Give the position of every Plasmodium parasite, noting whether each is a trophozoite, schizont, or gametocyte.
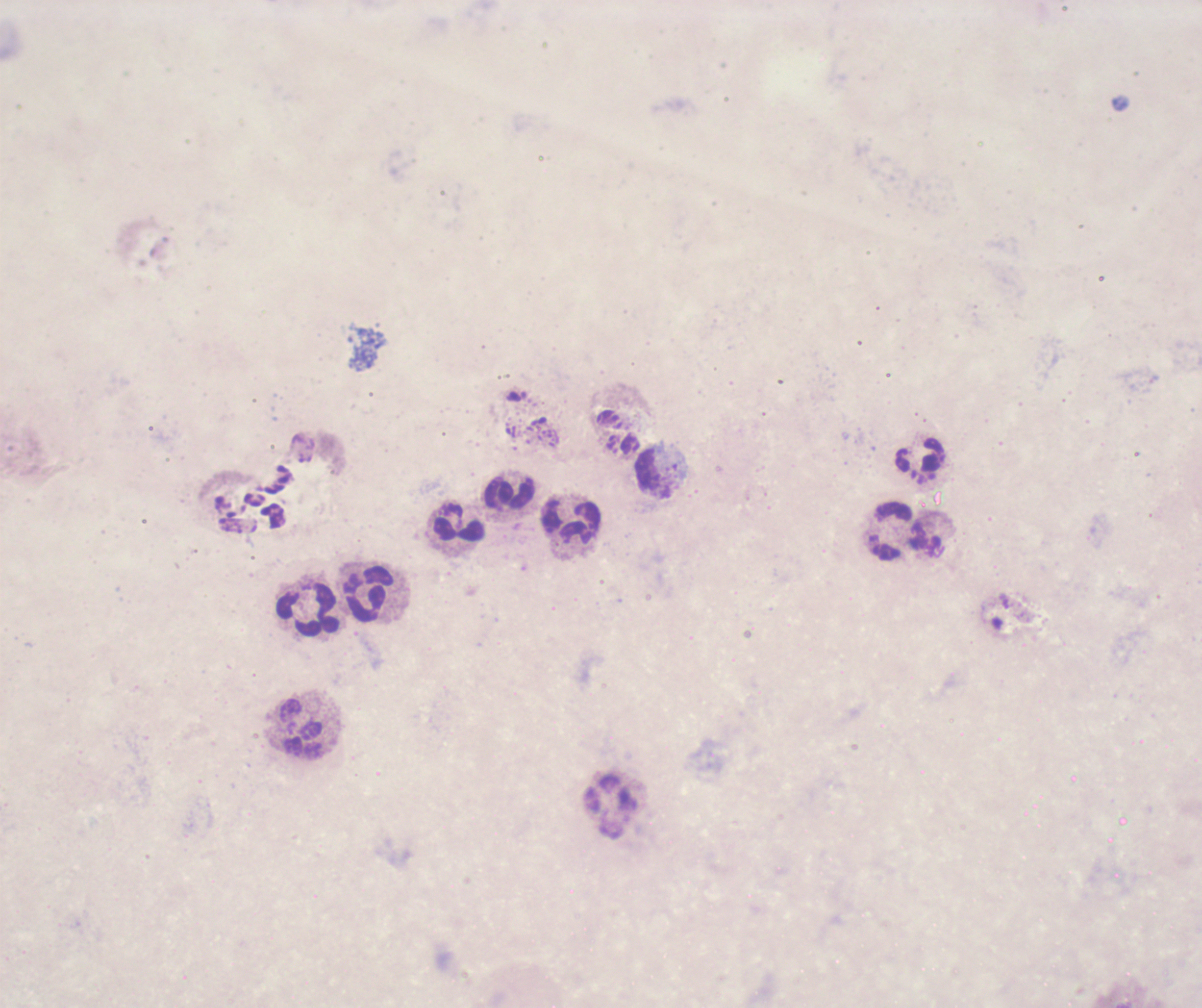
No Plasmodium parasites seen.

Approximate centers as [x, y] in pixels.
Summary:
  - Leukocyte locations: [921, 459], [654, 473], [509, 493], [573, 520], [459, 529], [892, 531], [370, 595], [310, 611], [302, 728], [610, 806]
  - Stain: Romanowsky
  - Field of view: one from this slide
  - Preparation: thick blood film
  - Coloration quality: bad
  - Magnification: 100x
  - Background quality: poor
  - Image size: 1202×1008 pixels
  - Context: previously used in a real diagnosis